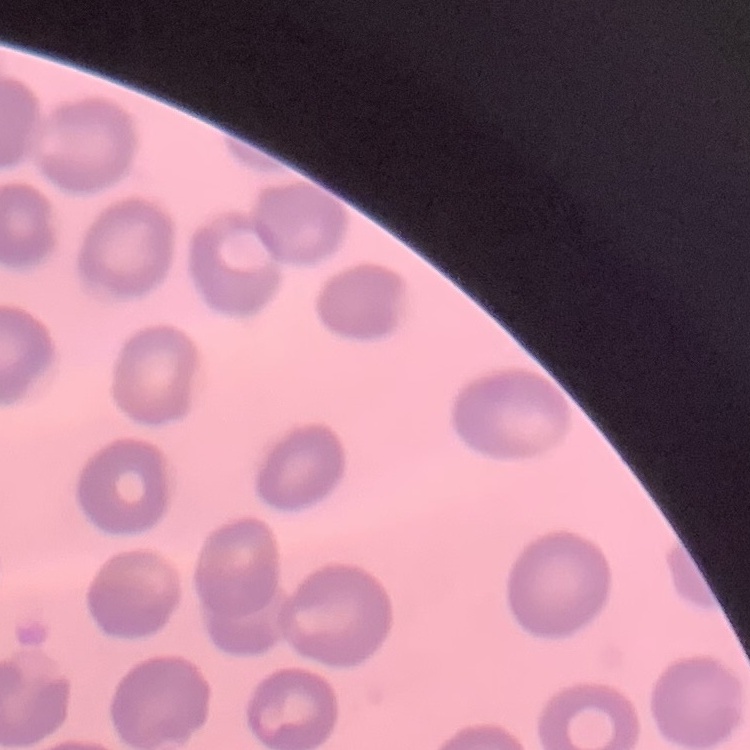 The erythrocytes exhibit no rouleaux formation. One tile cut from a larger photomicrograph. Stained with either Field's or Giemsa. Thin blood film.